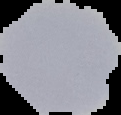
Malaria status: uninfected. From a thin blood film. Image is 121×115 pixels. Segmented cell region on a black background.